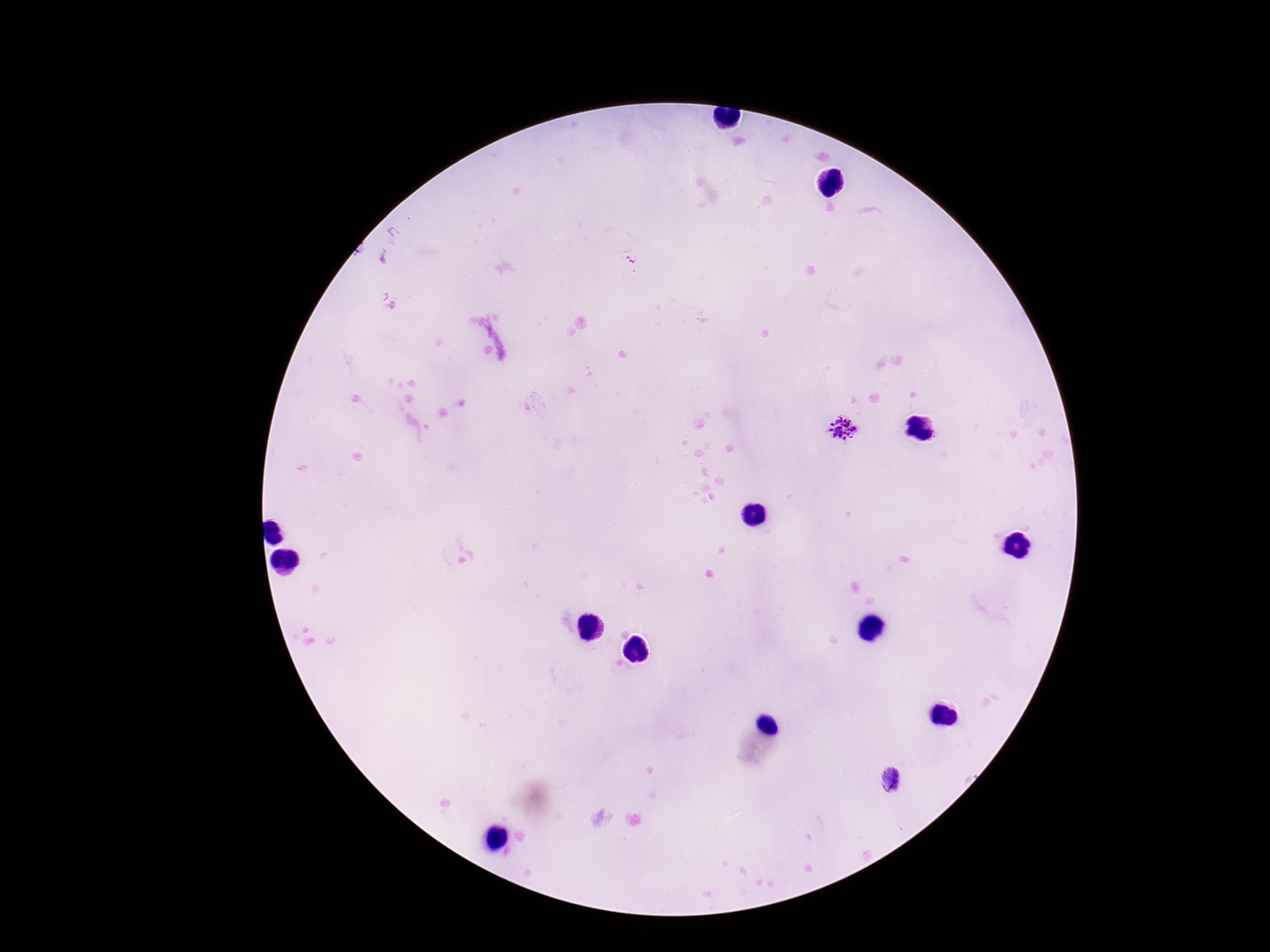
Approximate centers as (x, y) in pixels. Plasmodium parasite locations: (632, 258), (844, 429), (892, 780). Thick blood smear. Giemsa-stained preparation. Smartphone photograph taken through the microscope eyepiece. Image is 1270×952 pixels. Patient malaria status: infected. Single field of view. 100x magnification.